Name the blood parasite species.
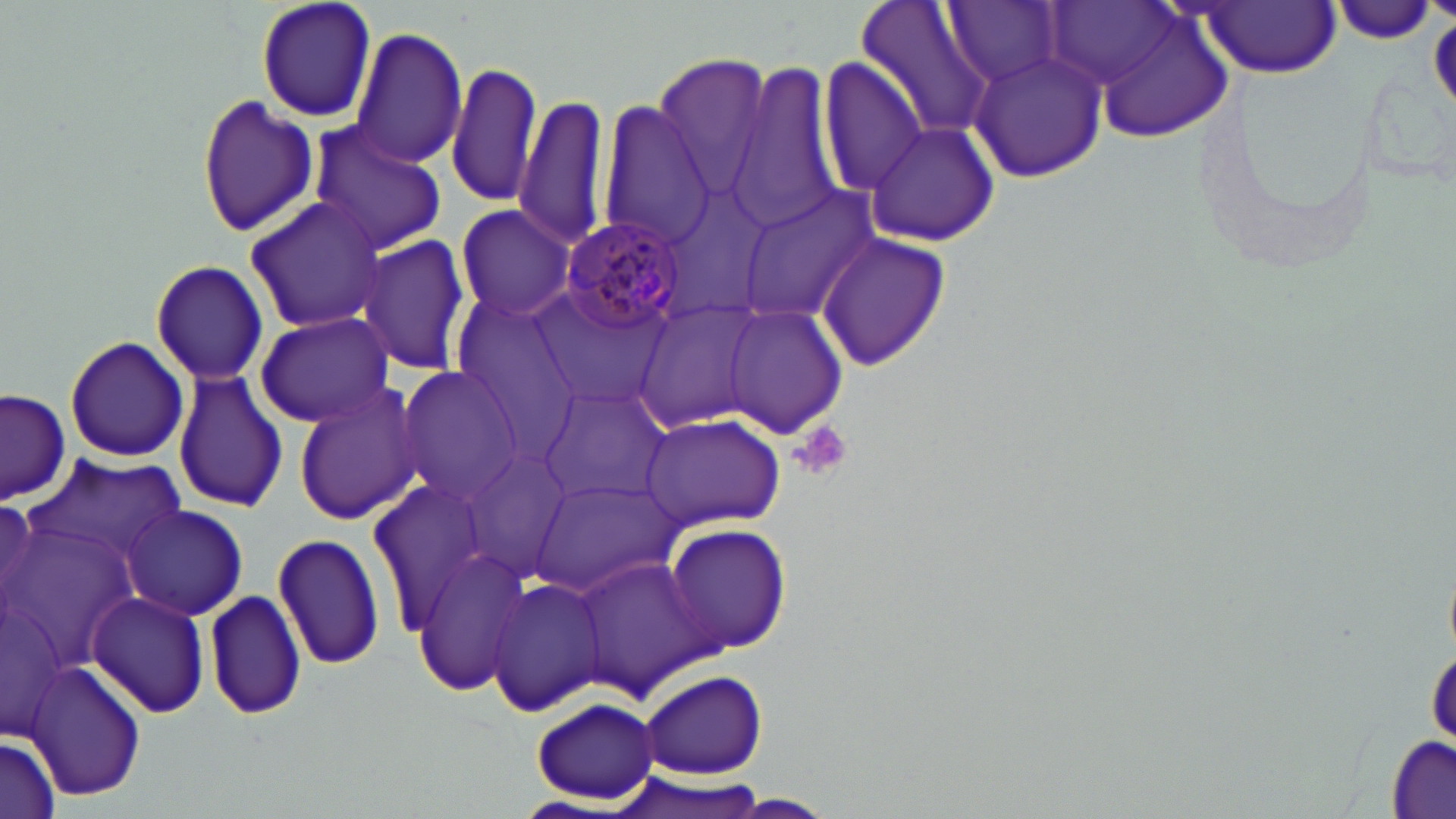

Plasmodium malariae.

Approximate bounding boxes as (x1,y1)-(x2,y2) corner pairs in pixels. Platelet locations: (791,420)-(852,484). Uninfected red blood cell locations: (257,0)-(378,122), (855,0)-(997,148), (943,2)-(1061,89), (1200,2)-(1339,77), (1330,2)-(1439,46), (1062,4)-(1243,144), (347,26)-(469,169), (967,49)-(1106,183), (651,53)-(773,194), (819,57)-(927,195), (726,60)-(844,232), (446,62)-(542,208), (194,92)-(319,239), (513,94)-(611,248), (594,98)-(716,250), (308,119)-(448,254), (863,122)-(1000,248), (739,187)-(879,319), (244,195)-(385,333), (454,205)-(577,319), (814,234)-(951,371), (358,236)-(470,377), (150,259)-(268,386), (531,287)-(671,408), (449,291)-(579,424), (632,299)-(767,435), (723,303)-(849,437), (252,311)-(394,428), (64,335)-(190,464), (393,366)-(523,505), (172,370)-(290,511), (292,385)-(424,526), (536,386)-(672,508), (1,388)-(71,506), (641,413)-(785,529), (26,455)-(183,564), (366,478)-(503,629), (536,478)-(682,599), (121,504)-(249,620), (6,515)-(137,677), (661,522)-(795,658), (272,528)-(384,673), (409,547)-(531,696), (573,554)-(715,701), (489,575)-(609,719), (3,582)-(64,742), (205,587)-(306,721), (89,591)-(210,719), (1428,636)-(1455,750), (25,660)-(149,802), (635,669)-(769,781), (531,696)-(661,802), (1387,734)-(1454,819), (0,738)-(60,819), (718,795)-(839,817). Plasmodium malariae-infected red blood cell locations: (560,216)-(691,332). May-Grünwald-Giemsa stain. Thin blood film. Image is 1456×819 pixels. Single field of view. Captured at 1000x magnification. Optical microscopy.